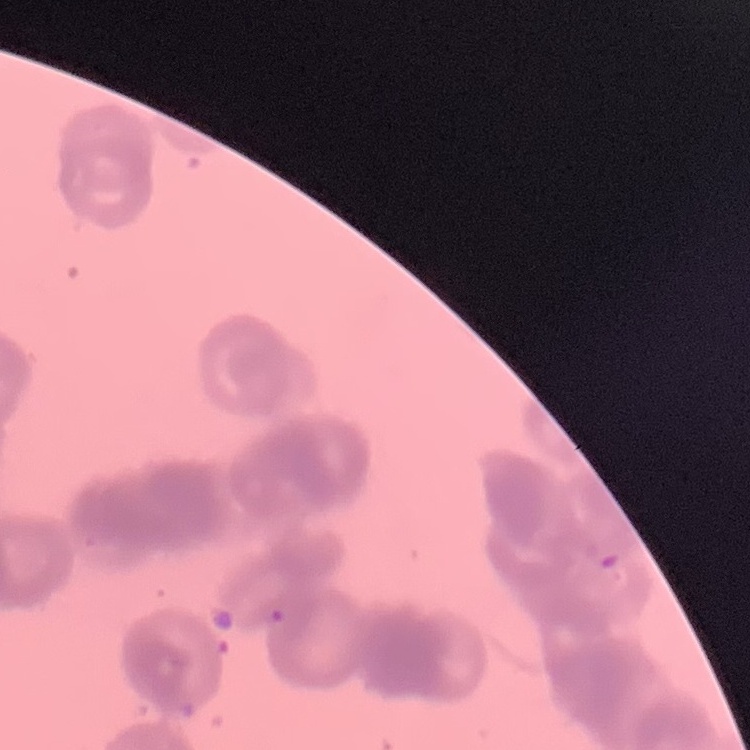

Summary:
  - Erythrocyte morphology: rouleaux formation
  - Stain: Field's or Giemsa
  - Preparation: thin blood smear
  - Image type: one tile cut from a larger photomicrograph